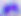
identification = Toxoplasma gondii
magnification = 400x
modality = micrograph